Comment on the morphology of the erythrocytes.
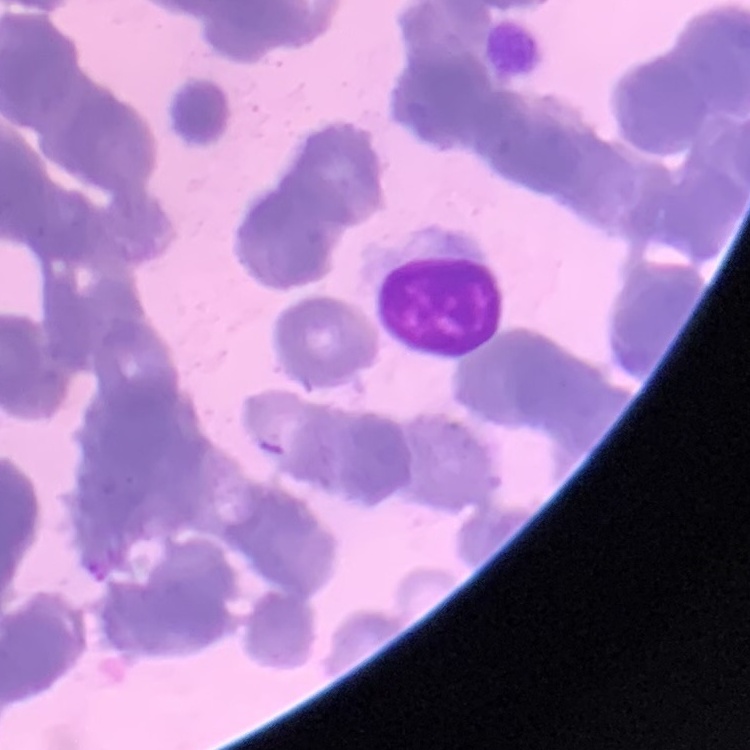
Rouleaux formation.

{
  "image_type": "square crop of a larger photomicrograph",
  "stain": "Field's or Giemsa",
  "preparation": "thin blood smear"
}